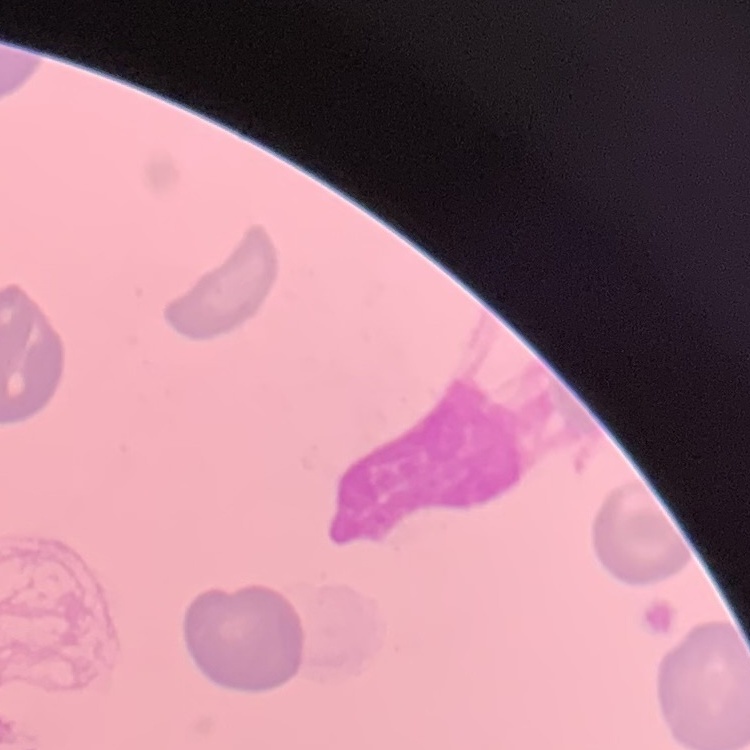

red_blood_cell_morphology: no rouleaux formation
preparation: thin blood smear
stain: Field's or Giemsa
image_type: one tile cut from a larger photomicrograph